Assess this cell for malaria.
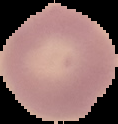

Uninfected.

image_size: 118×124 pixels
preparation: thin blood film
image_type: cell region segmented out of the field of view; surrounding area masked to black